Classify this cell by malaria status.
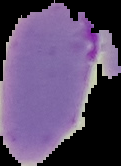

Parasitized.

Image is 121×166 pixels. From a thin blood film. The area outside the segmented cell region is set to black.